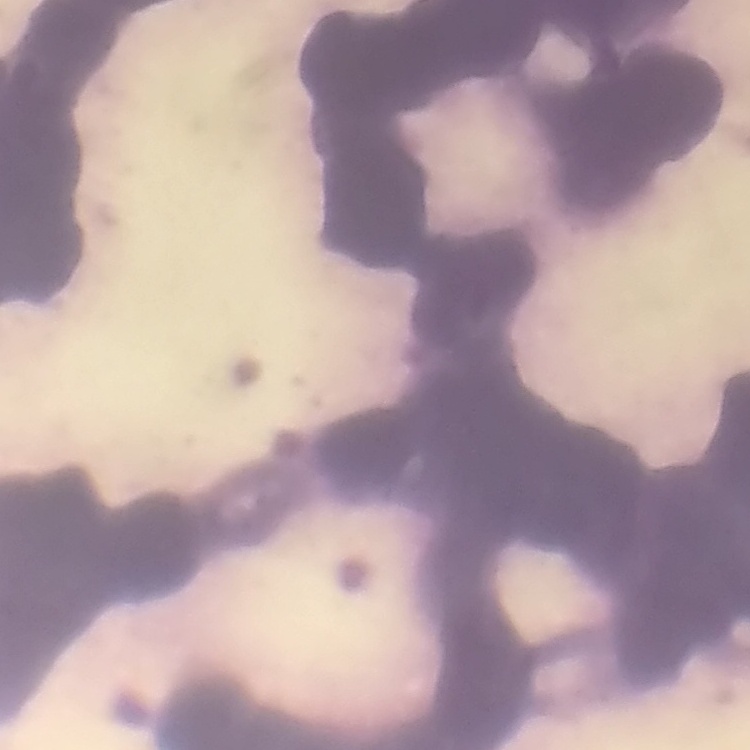

The red blood cells show rouleaux formation. One tile cut from a larger photomicrograph. Thin blood smear. Field's or Giemsa stain.